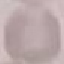

result = no malaria parasites seen
image type = automatically extracted cell patch, resized to 64 × 64 pixels
stain = Giemsa
preparation = thin blood film
capture = smartphone camera at the microscope eyepiece